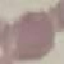
Summary:
  - Result: no malaria parasites detected
  - Preparation: thin blood film
  - Capture: smartphone through the microscope eyepiece
  - Stain: Giemsa
  - Image type: automatically extracted cell patch, resized to 64 × 64 pixels